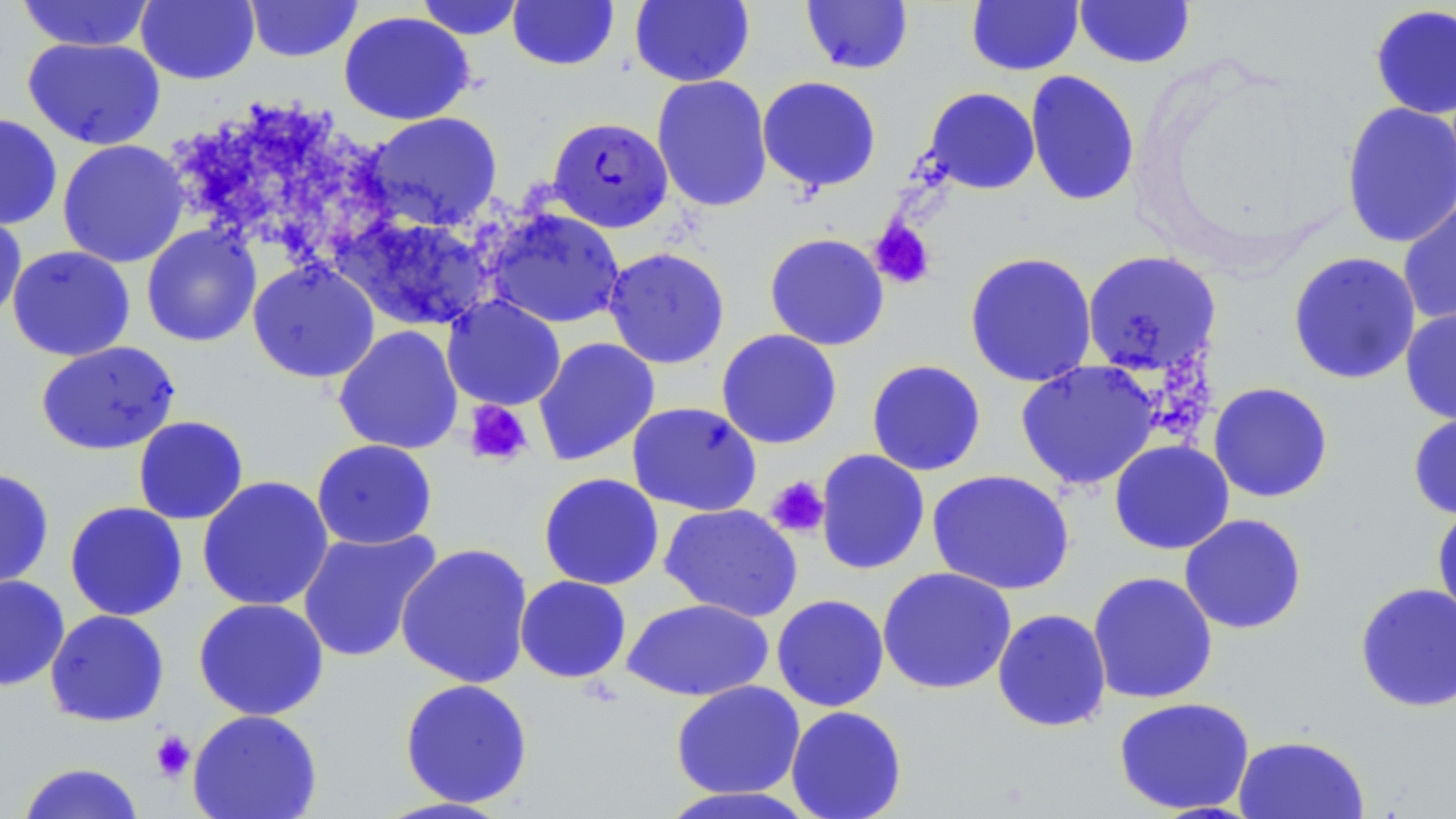 Approximate bounding boxes as (x1, y1, x2, y2) in pixels. Uninfected red blood cell locations: (16, 0, 155, 52), (136, 0, 259, 85), (415, 0, 526, 40), (507, 0, 620, 72), (630, 0, 754, 87), (800, 0, 914, 75), (1074, 0, 1195, 69), (245, 1, 362, 63), (966, 1, 1084, 76), (1369, 4, 1456, 120), (338, 11, 475, 125), (22, 37, 165, 150), (1025, 70, 1140, 207), (651, 74, 773, 212), (757, 76, 882, 193), (923, 87, 1040, 195), (1339, 101, 1456, 249), (363, 111, 503, 230), (0, 114, 63, 230), (57, 139, 190, 268), (1398, 192, 1456, 328), (0, 205, 27, 325), (484, 209, 626, 330), (331, 210, 498, 333), (141, 225, 262, 347), (764, 233, 890, 351), (7, 245, 136, 361), (603, 247, 730, 369), (1082, 249, 1222, 376), (964, 251, 1098, 388), (1287, 251, 1421, 385), (248, 259, 380, 383), (441, 295, 566, 411), (1400, 306, 1456, 425), (333, 325, 464, 455), (716, 329, 842, 449), (533, 337, 660, 466), (35, 341, 180, 456), (866, 359, 986, 476), (1015, 360, 1161, 491), (1208, 382, 1334, 503), (627, 402, 762, 517), (1407, 407, 1456, 521), (133, 415, 249, 525), (311, 439, 438, 550), (1109, 439, 1234, 555), (815, 449, 930, 575), (0, 467, 55, 591), (927, 469, 1076, 596), (538, 472, 664, 591), (196, 476, 334, 612), (64, 501, 188, 621), (1431, 502, 1456, 626), (659, 503, 803, 622), (1179, 513, 1307, 635), (297, 528, 442, 663), (395, 542, 534, 689), (876, 567, 1017, 695), (1087, 571, 1218, 705), (0, 574, 70, 691), (515, 575, 632, 684), (1354, 582, 1456, 712), (771, 594, 890, 712), (192, 597, 330, 721), (621, 598, 775, 702), (992, 608, 1112, 732), (45, 609, 170, 727), (398, 678, 534, 808), (670, 680, 806, 799), (1113, 697, 1255, 815), (785, 705, 908, 819), (187, 709, 323, 819), (1232, 734, 1370, 819), (16, 761, 146, 819), (657, 786, 819, 819), (374, 796, 516, 818). Platelet locations: (869, 219, 936, 290), (463, 400, 533, 467), (765, 476, 830, 538), (149, 729, 196, 783). Plasmodium falciparum-infected red blood cell locations: (547, 117, 673, 233). Slide-level diagnosis: Plasmodium falciparum. One field of a larger specimen. May-Grünwald-Giemsa stain. Image is 1456×819 pixels. Optical microscopy. Thin blood film. 1000x magnification.